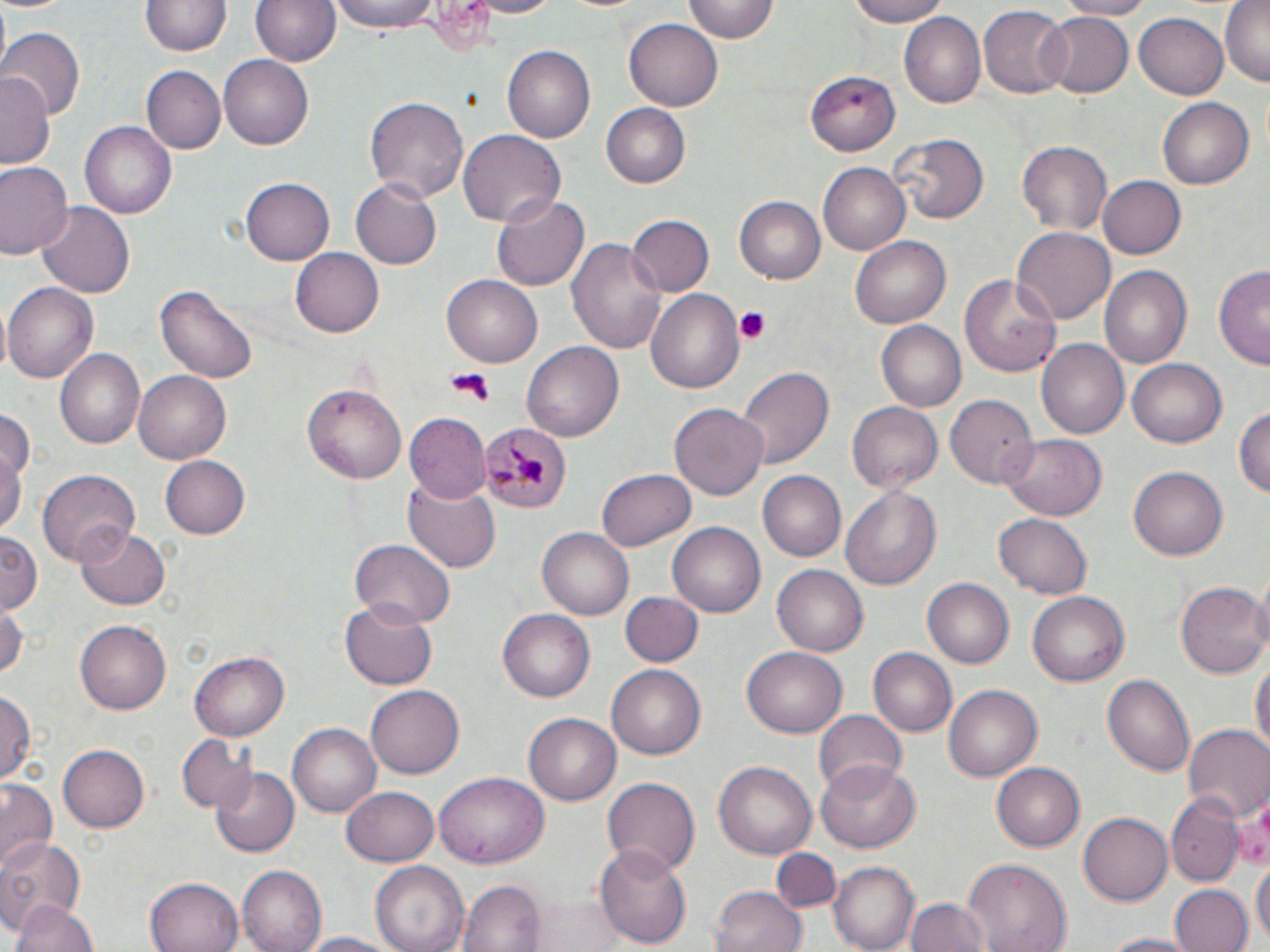
Summary:
  - Coordinate format: approximate bounding boxes as (x1, y1, x2, y2) in pixels
  - Platelet locations: (732, 305, 773, 343), (443, 370, 494, 404)
  - Plasmodium malariae-infected red blood cell locations: (480, 422, 571, 513)
  - Uninfected red blood cell locations: (0, 0, 75, 16), (252, 0, 338, 67), (330, 0, 442, 35), (467, 0, 565, 18), (681, 0, 779, 43), (839, 0, 958, 26), (1053, 0, 1157, 20), (1220, 0, 1269, 86), (140, 2, 230, 58), (978, 5, 1068, 99), (1038, 11, 1132, 98), (1134, 11, 1228, 100), (899, 12, 986, 109), (624, 18, 723, 109), (0, 28, 83, 122), (502, 45, 594, 142), (219, 55, 313, 149), (140, 65, 224, 151), (0, 71, 53, 168), (809, 71, 899, 157), (364, 95, 468, 204), (1157, 98, 1254, 188), (600, 104, 688, 189), (82, 121, 176, 219), (457, 128, 565, 228), (892, 135, 988, 224), (1017, 140, 1114, 236), (0, 162, 72, 261), (818, 164, 909, 254), (1095, 175, 1185, 260), (242, 177, 334, 265), (352, 180, 442, 270), (492, 193, 591, 293), (736, 197, 826, 284), (37, 202, 133, 300), (628, 216, 714, 295), (1011, 227, 1116, 326), (569, 234, 665, 357), (850, 235, 948, 327), (291, 248, 384, 337), (1098, 264, 1192, 369), (1215, 265, 1269, 369), (959, 274, 1061, 378), (442, 277, 542, 367), (3, 282, 99, 383), (156, 286, 258, 383), (644, 287, 745, 395), (878, 321, 965, 410), (1037, 339, 1130, 440), (521, 341, 623, 443), (55, 349, 145, 448), (1128, 357, 1226, 448), (737, 367, 834, 468), (134, 371, 231, 463), (301, 384, 408, 485), (945, 392, 1036, 488), (847, 400, 943, 491), (671, 404, 768, 502), (0, 405, 33, 488), (1233, 405, 1270, 501), (407, 415, 490, 502), (1001, 433, 1107, 520), (0, 441, 24, 537), (159, 454, 249, 541), (1130, 466, 1227, 561), (38, 470, 138, 565), (756, 470, 846, 562), (598, 471, 694, 550), (404, 481, 500, 575), (838, 483, 941, 591), (993, 511, 1091, 598), (668, 522, 766, 618), (75, 525, 170, 611), (538, 526, 636, 621), (0, 531, 43, 615), (353, 541, 455, 628), (772, 565, 868, 656), (923, 577, 1016, 669), (1177, 581, 1269, 680), (1027, 589, 1132, 687), (621, 590, 700, 666), (339, 596, 437, 690), (0, 603, 25, 680), (497, 608, 596, 702), (74, 619, 171, 715), (742, 644, 850, 738), (868, 648, 956, 738), (190, 651, 291, 739), (1252, 657, 1269, 765), (607, 665, 705, 760), (1103, 673, 1196, 780), (943, 684, 1042, 781), (366, 686, 465, 780), (0, 690, 35, 785), (814, 711, 907, 796), (523, 713, 620, 805), (290, 723, 384, 816), (1184, 726, 1270, 822), (177, 733, 255, 815), (57, 744, 149, 833), (992, 760, 1086, 850), (712, 761, 817, 860), (816, 761, 920, 853), (213, 768, 298, 856), (434, 772, 549, 868), (601, 776, 700, 877), (0, 781, 58, 868), (342, 786, 438, 867), (1168, 794, 1243, 886), (1234, 795, 1270, 874), (1079, 814, 1172, 905), (0, 836, 84, 931), (595, 842, 692, 949), (770, 848, 840, 911), (1251, 858, 1269, 947), (961, 860, 1073, 952), (371, 862, 469, 952), (830, 863, 918, 950), (238, 864, 329, 952), (146, 877, 245, 952), (459, 879, 544, 952), (710, 885, 807, 952), (1170, 885, 1251, 952), (13, 897, 97, 952), (905, 897, 989, 952), (531, 898, 633, 951), (300, 931, 403, 952), (1096, 932, 1206, 952)
  - Slide-level diagnosis: Plasmodium malariae
  - Stain: May-Grünwald-Giemsa
  - Modality: optical microscopy
  - Magnification: 1000x
  - Field of view: single
  - Image size: 1270×952 pixels
  - Preparation: thin blood smear